Assess this cell for malaria.
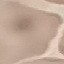

It is uninfected.

image_type: cell patch, automatically extracted from a larger field of view and resized to 64 × 64 pixels
capture: smartphone through the microscope eyepiece
preparation: thin blood smear
stain: Giemsa